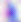

400x magnification. Toxoplasma gondii is seen. Micrograph.